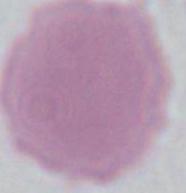

Summary:
  - Modality: photomicrograph
  - Identification: red blood cell
  - Magnification: 1000x